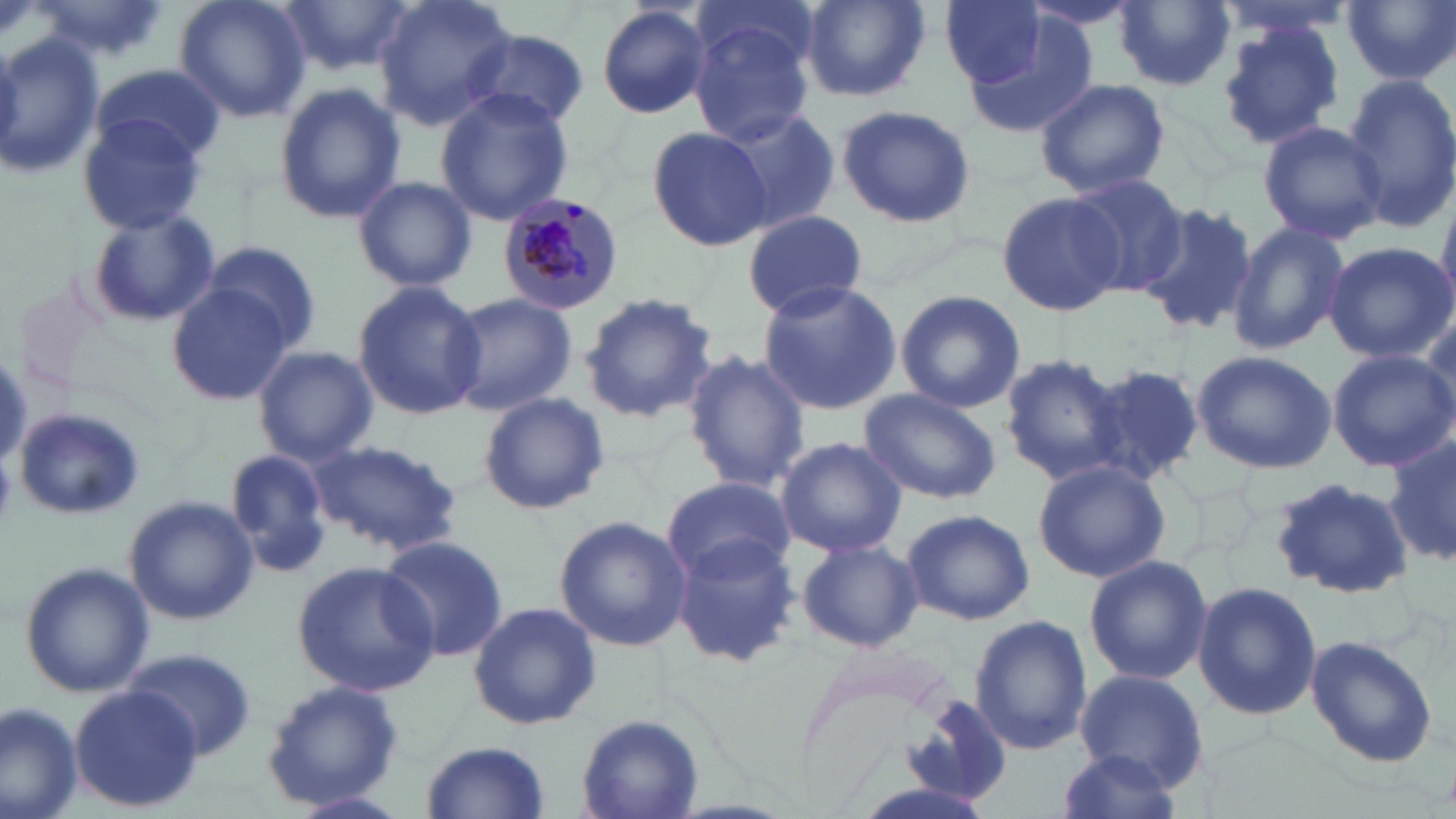
slide-level diagnosis = Plasmodium malariae
preparation = thin blood film
stain = May-Grünwald-Giemsa
field of view = single
magnification = 1000x
image size = 1456×819 pixels
modality = optical microscopy
Plasmodium malariae-infected red blood cell locations = approximate bounding boxes as named x1/y1/x2/y2 corners in pixels: (x1=496, y1=192, x2=626, y2=317)
uninfected red blood cell locations = approximate bounding boxes as named x1/y1/x2/y2 corners in pixels: (x1=30, y1=0, x2=170, y2=67), (x1=174, y1=0, x2=312, y2=123), (x1=281, y1=0, x2=413, y2=75), (x1=371, y1=0, x2=518, y2=132), (x1=799, y1=0, x2=930, y2=103), (x1=939, y1=0, x2=1050, y2=90), (x1=1211, y1=0, x2=1366, y2=39), (x1=1344, y1=0, x2=1456, y2=85), (x1=1115, y1=1, x2=1236, y2=91), (x1=594, y1=3, x2=713, y2=122), (x1=952, y1=10, x2=1101, y2=139), (x1=689, y1=18, x2=813, y2=146), (x1=1213, y1=21, x2=1347, y2=151), (x1=464, y1=32, x2=588, y2=128), (x1=0, y1=33, x2=105, y2=180), (x1=92, y1=63, x2=225, y2=165), (x1=1342, y1=75, x2=1455, y2=231), (x1=1034, y1=78, x2=1169, y2=200), (x1=273, y1=83, x2=406, y2=223), (x1=434, y1=89, x2=575, y2=223), (x1=834, y1=101, x2=977, y2=228), (x1=715, y1=106, x2=841, y2=236), (x1=75, y1=113, x2=207, y2=236), (x1=1257, y1=119, x2=1387, y2=244), (x1=646, y1=126, x2=772, y2=250), (x1=1061, y1=172, x2=1191, y2=296), (x1=351, y1=175, x2=478, y2=293), (x1=998, y1=193, x2=1122, y2=318), (x1=1137, y1=199, x2=1258, y2=336), (x1=742, y1=209, x2=867, y2=319), (x1=86, y1=210, x2=220, y2=329), (x1=1226, y1=223, x2=1350, y2=356), (x1=201, y1=240, x2=320, y2=354), (x1=1323, y1=242, x2=1453, y2=363), (x1=167, y1=280, x2=299, y2=404), (x1=757, y1=280, x2=901, y2=416), (x1=351, y1=281, x2=485, y2=420), (x1=895, y1=289, x2=1025, y2=413), (x1=441, y1=291, x2=578, y2=416), (x1=578, y1=291, x2=719, y2=425), (x1=253, y1=347, x2=377, y2=464), (x1=1192, y1=349, x2=1337, y2=474), (x1=680, y1=350, x2=808, y2=495), (x1=1327, y1=350, x2=1454, y2=468), (x1=999, y1=353, x2=1131, y2=486), (x1=1086, y1=361, x2=1206, y2=485), (x1=858, y1=389, x2=1001, y2=503), (x1=478, y1=391, x2=608, y2=515), (x1=14, y1=406, x2=146, y2=518), (x1=1385, y1=426, x2=1456, y2=572), (x1=775, y1=436, x2=907, y2=556), (x1=310, y1=440, x2=464, y2=556), (x1=224, y1=449, x2=334, y2=575), (x1=1031, y1=459, x2=1171, y2=583), (x1=662, y1=476, x2=797, y2=584), (x1=1272, y1=476, x2=1413, y2=601), (x1=124, y1=494, x2=260, y2=625), (x1=902, y1=508, x2=1034, y2=626), (x1=555, y1=516, x2=693, y2=652), (x1=374, y1=534, x2=509, y2=664), (x1=667, y1=534, x2=802, y2=669), (x1=797, y1=539, x2=923, y2=653), (x1=1083, y1=553, x2=1213, y2=686), (x1=294, y1=559, x2=441, y2=697), (x1=19, y1=562, x2=154, y2=698), (x1=1192, y1=580, x2=1321, y2=723), (x1=469, y1=601, x2=601, y2=730), (x1=969, y1=615, x2=1091, y2=757), (x1=1305, y1=635, x2=1439, y2=768), (x1=123, y1=649, x2=258, y2=762), (x1=1074, y1=668, x2=1208, y2=791), (x1=262, y1=680, x2=403, y2=809), (x1=69, y1=686, x2=201, y2=811), (x1=902, y1=694, x2=1014, y2=806), (x1=0, y1=701, x2=84, y2=819), (x1=577, y1=713, x2=704, y2=817), (x1=421, y1=741, x2=550, y2=818), (x1=1053, y1=750, x2=1186, y2=819)